State which cell type is depicted.
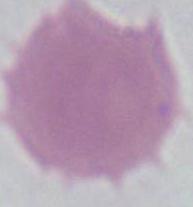

This is an erythrocyte.

Captured at 1000x magnification. Micrograph.